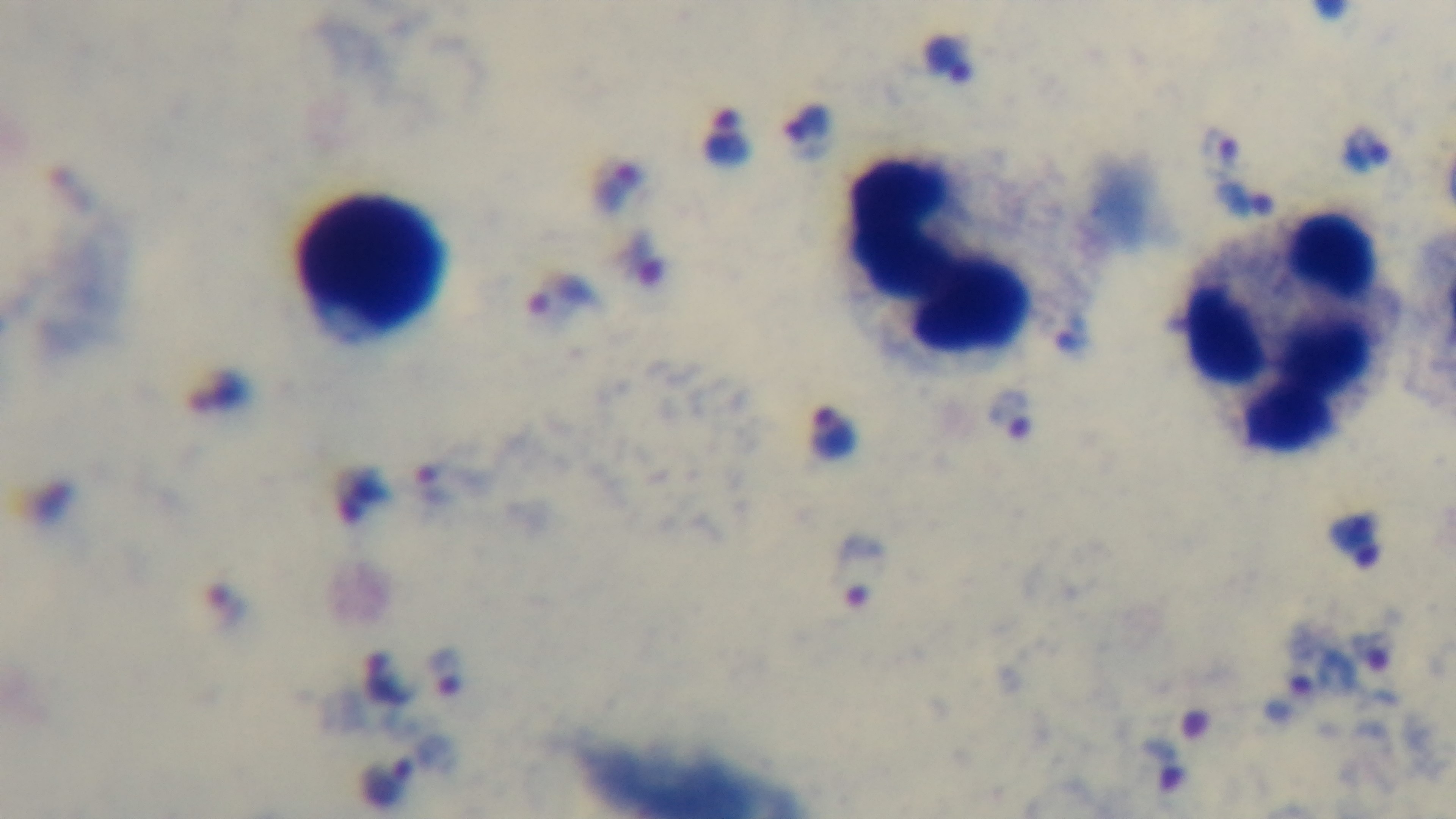

Single field of view. Giemsa stain. Captured with a mounted 4K digital camera. Preparation: thick blood film. Malaria status: infected. Photomicrograph. Oil-immersion objective, 100x.